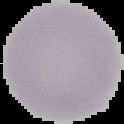

The area outside the segmented cell region is set to black. From a thin blood film. Malaria status: uninfected. Image is 124×124 pixels.